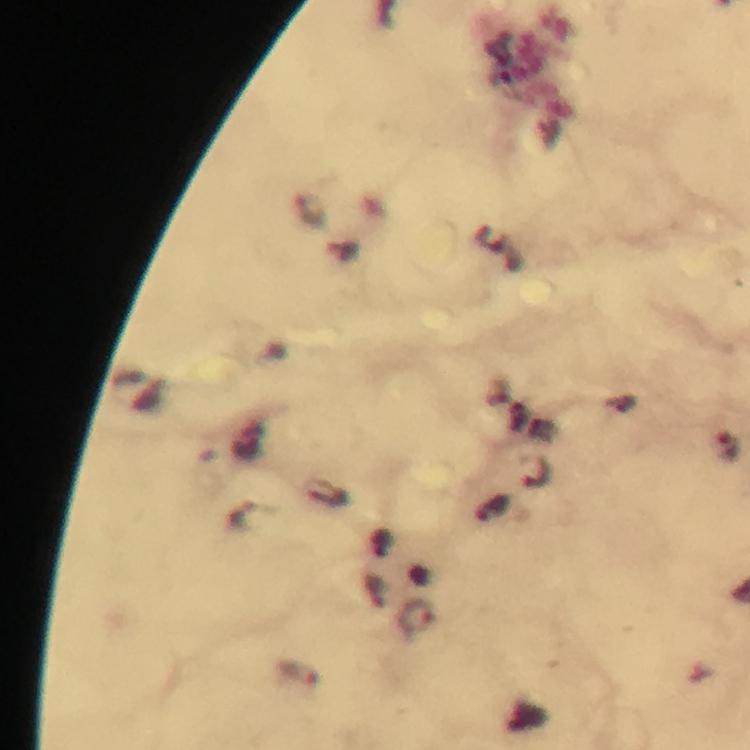

cropped from = one field of view
preparation = thick smear
stain = Giemsa
image size = 750×750 pixels
malaria parasite locations = approximate centers as {x, y} in pixels: {730, 447}, {250, 516}, {417, 616}, {301, 675}
context = from a malaria diagnostic workup
immersion oil = used
capture = smartphone mounted on the microscope
magnification = 100x